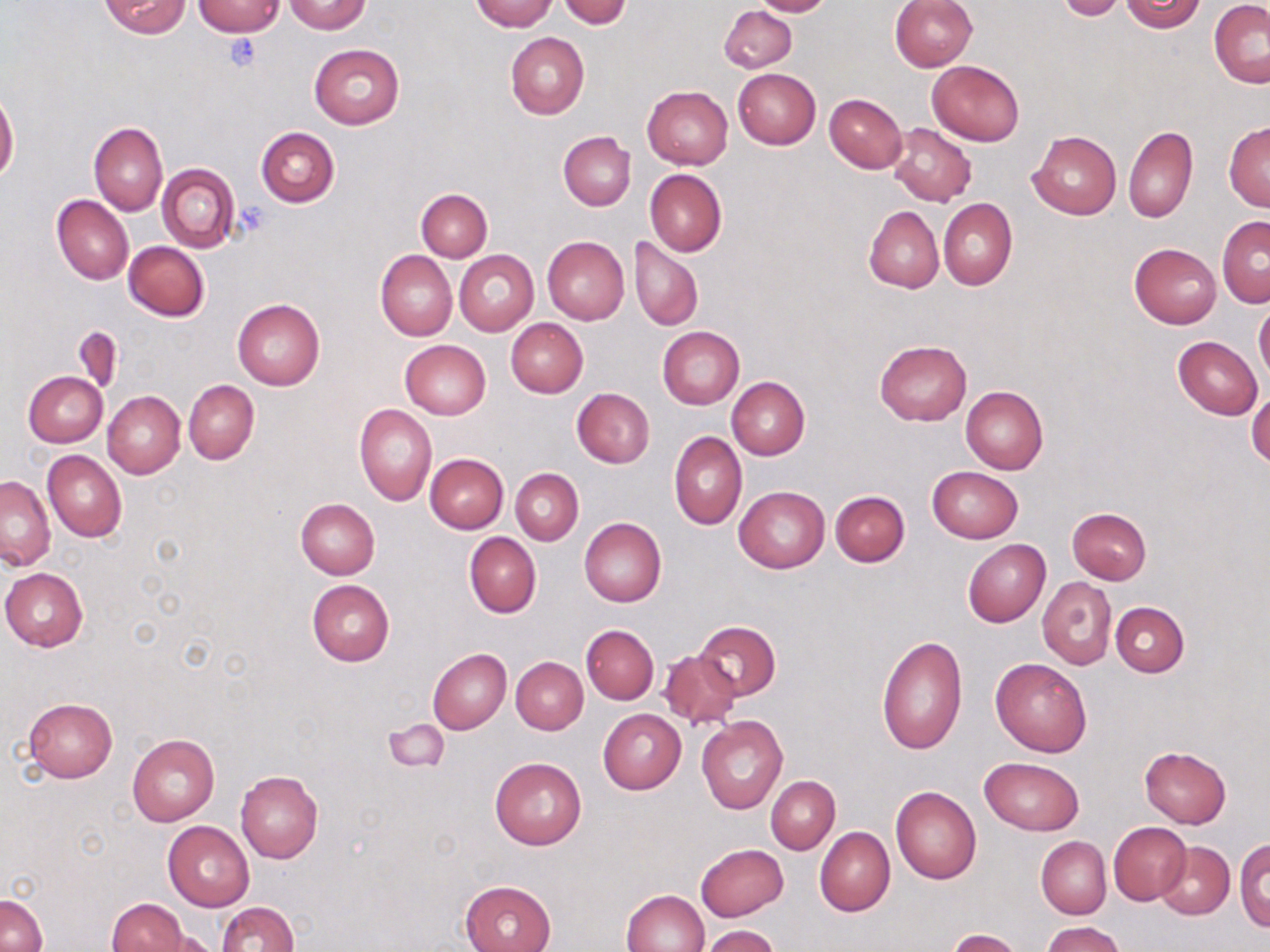
Summary:
  - Coordinate format: approximate bounding boxes as [x1, y1, x2, y2] in pixels
  - Platelet locations: [223, 32, 263, 71], [234, 202, 270, 240]
  - Uninfected red blood cell locations: [98, 0, 191, 39], [469, 0, 557, 31], [559, 0, 631, 28], [750, 0, 833, 17], [889, 0, 977, 70], [1117, 0, 1206, 32], [1209, 0, 1270, 87], [193, 1, 285, 36], [284, 1, 372, 33], [1055, 1, 1127, 21], [719, 5, 797, 73], [505, 32, 589, 120], [309, 44, 404, 129], [926, 59, 1024, 145], [733, 68, 821, 149], [641, 86, 732, 170], [0, 91, 19, 185], [824, 93, 907, 172], [1224, 121, 1270, 210], [89, 122, 168, 216], [886, 122, 976, 206], [1123, 126, 1198, 224], [256, 127, 339, 207], [559, 131, 636, 209], [1028, 131, 1122, 220], [156, 163, 240, 253], [645, 169, 726, 256], [416, 188, 492, 261], [52, 196, 133, 286], [939, 199, 1017, 290], [863, 207, 943, 293], [1216, 216, 1270, 306], [541, 237, 629, 325], [630, 237, 702, 331], [123, 242, 209, 321], [1129, 243, 1221, 326], [375, 250, 457, 341], [455, 250, 538, 336], [233, 299, 325, 390], [1254, 303, 1270, 382], [505, 317, 588, 397], [73, 325, 124, 393], [657, 327, 743, 409], [1173, 336, 1263, 419], [400, 340, 491, 419], [874, 340, 970, 426], [24, 371, 108, 447], [726, 377, 809, 459], [184, 380, 259, 465], [960, 384, 1048, 475], [572, 387, 655, 468], [1247, 390, 1270, 468], [103, 391, 185, 478], [354, 404, 437, 506], [669, 430, 747, 530], [42, 450, 126, 543], [424, 454, 507, 534], [927, 466, 1024, 542], [510, 468, 582, 545], [1, 475, 54, 569], [734, 486, 829, 573], [829, 491, 909, 566], [296, 498, 379, 578], [1067, 508, 1151, 584], [579, 518, 667, 607], [464, 532, 541, 619], [963, 539, 1050, 627], [2, 567, 87, 651], [1036, 577, 1116, 670], [307, 580, 394, 666], [1111, 602, 1189, 677], [693, 621, 781, 700], [582, 625, 659, 703], [875, 635, 967, 755], [427, 649, 511, 734], [660, 650, 742, 730], [511, 656, 587, 734], [990, 657, 1093, 757], [24, 697, 118, 782], [598, 709, 686, 794], [696, 716, 788, 815], [383, 718, 448, 772], [128, 733, 220, 825], [1139, 746, 1232, 828], [981, 756, 1083, 834], [490, 757, 585, 850], [235, 771, 323, 862], [766, 775, 840, 853], [890, 786, 982, 884], [163, 821, 254, 911], [1107, 821, 1191, 905], [814, 826, 895, 917], [1036, 837, 1110, 919], [1235, 839, 1269, 932], [1155, 842, 1235, 919], [695, 844, 788, 921], [461, 880, 556, 952], [622, 889, 709, 952], [0, 893, 46, 952], [106, 899, 189, 951], [216, 901, 299, 952], [1042, 921, 1123, 952], [702, 925, 781, 952], [949, 929, 1024, 952], [144, 931, 218, 952]
  - Slide-level diagnosis: no evidence of blood parasites
  - Field of view: single
  - Image size: 1270×952 pixels
  - Magnification: 1000x
  - Preparation: thin blood film
  - Modality: light microscopy
  - Stain: May-Grünwald-Giemsa